Assess this cell for malaria.
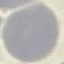
It is uninfected.

Summary:
  - Image type: cell patch, automatically extracted from a larger field of view and resized to 64 × 64 pixels
  - Stain: Giemsa
  - Capture: smartphone camera at the microscope eyepiece
  - Preparation: thin smear